Report the malaria status of this cell.
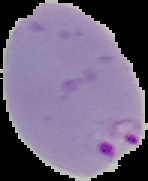
Parasitized.

Summary:
  - Preparation: thin blood smear
  - Image type: cell region segmented out of the field of view; surrounding area masked to black
  - Image size: 148×181 pixels